Outline each uninfected red blood cell.
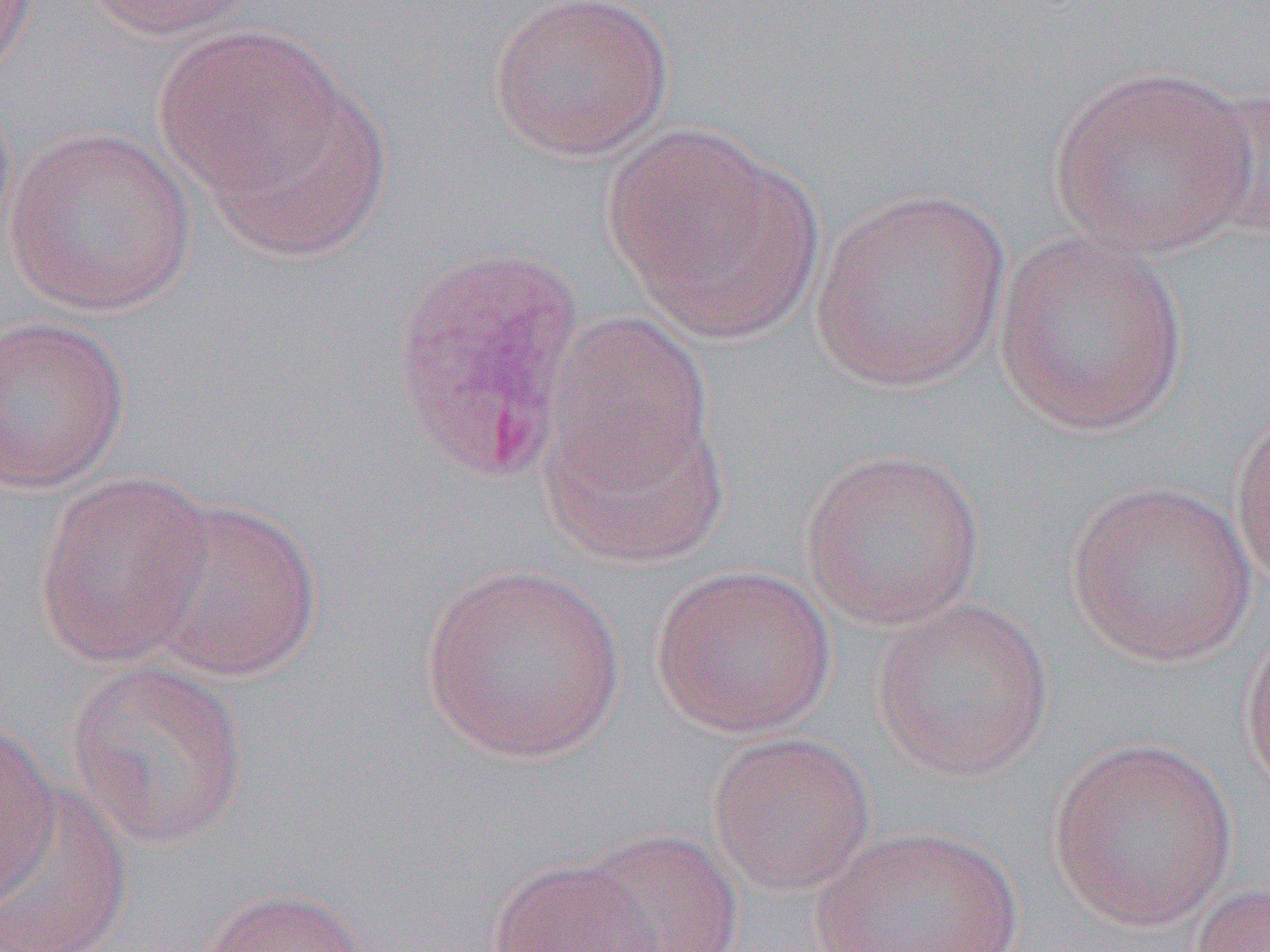

Approximate bounding boxes as (x1,y1)-(x2,y2) corner pairs in pixels.
Uninfected red blood cells: (0,0)-(40,80), (80,0)-(258,40), (487,0)-(675,162), (153,26)-(348,195), (1045,65)-(1260,257), (194,75)-(391,260), (1192,82)-(1270,243), (0,86)-(20,255), (605,124)-(823,341), (4,126)-(198,316), (810,186)-(1014,395), (992,231)-(1189,437), (543,312)-(717,501), (0,314)-(131,494), (541,394)-(729,567), (800,448)-(987,630), (33,469)-(217,669), (1065,477)-(1256,667), (139,495)-(324,682), (419,561)-(627,765), (649,564)-(837,738), (870,596)-(1056,782), (1238,622)-(1270,798), (64,659)-(249,850), (0,726)-(62,907), (707,732)-(876,895), (1047,735)-(1240,932), (1,783)-(133,952), (813,825)-(1026,952), (577,828)-(745,952), (489,857)-(663,952), (1187,880)-(1270,952), (201,887)-(369,952).

{
  "slide_level_diagnosis": "Plasmodium vivax",
  "modality": "light microscopy",
  "preparation": "thin blood film",
  "image_size": "1270×952 pixels",
  "field_of_view": "single",
  "magnification": "1000x"
}